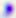

magnification = 400x
modality = photomicrograph
identification = Toxoplasma gondii